Evaluate for malaria.
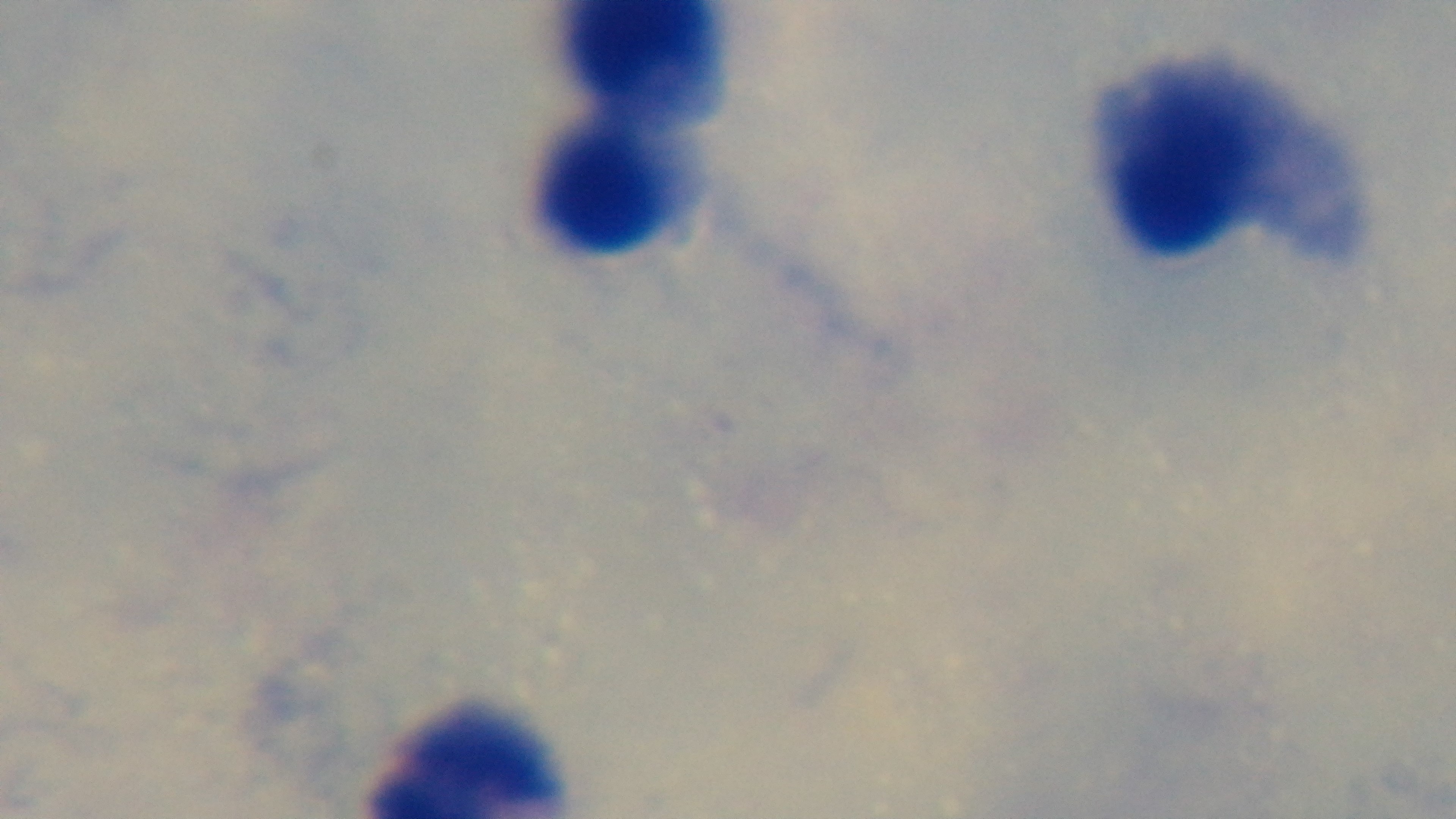
Uninfected.

Giemsa stain. Oil-immersion objective, 100x. Captured with a mounted 4K digital camera. One field from the slide. Photomicrograph. Preparation: thick.